Identify the blood parasite species.
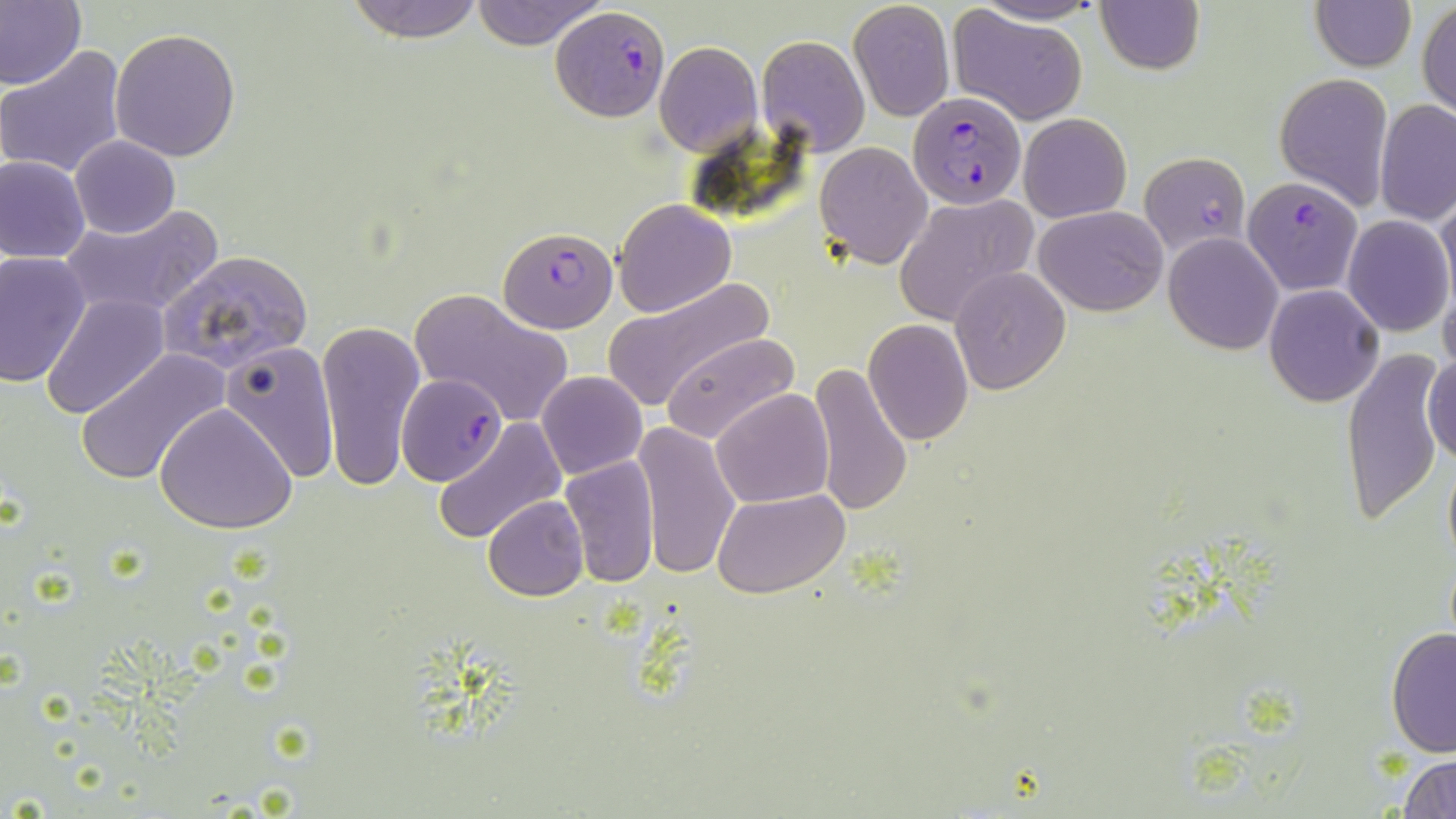

Plasmodium falciparum.

image_size: 1456×819 pixels
modality: optical microscopy
magnification: 1000x
stain: May-Grünwald-Giemsa
plasmodium_falciparum_infected_red_blood_cell_locations: 'approximate bounding boxes as (x1,y1)-(x2,y2) corner pairs in pixels: (553,9)-(668,122), (906,90)-(1027,210), (1139,152)-(1251,259), (1241,177)-(1363,294), (497,225)-(618,333), (398,373)-(506,485)'
preparation: thin blood film
field_of_view: single
uninfected_red_blood_cell_locations: 'approximate bounding boxes as (x1,y1)-(x2,y2) corner pairs in pixels: (0,0)-(85,92), (343,0)-(488,41), (469,0)-(604,48), (970,0)-(1105,25), (1095,0)-(1204,75), (1308,0)-(1416,71), (848,1)-(955,121), (1418,2)-(1455,121), (947,7)-(1091,126), (110,27)-(241,161), (755,34)-(869,156), (654,40)-(763,156), (0,46)-(129,179), (1276,72)-(1395,211), (1375,102)-(1456,226), (1018,112)-(1131,222), (69,137)-(179,239), (815,143)-(933,269), (1,155)-(90,264), (1437,192)-(1456,316), (893,195)-(1037,327), (612,198)-(737,318), (58,203)-(223,321), (1033,204)-(1169,315), (1341,214)-(1452,337), (1164,231)-(1284,355), (160,249)-(314,372), (0,251)-(93,389), (949,266)-(1071,393), (604,276)-(774,412), (1438,278)-(1456,381), (1264,284)-(1383,406), (410,288)-(571,425), (40,295)-(168,422), (316,319)-(426,492), (863,319)-(973,445), (660,332)-(800,446), (220,339)-(339,481), (1341,347)-(1446,529), (77,348)-(230,488), (1424,349)-(1456,469), (808,361)-(913,518), (535,370)-(648,480), (712,388)-(834,510), (154,403)-(296,535), (433,419)-(567,544), (633,421)-(741,582), (1441,451)-(1456,570), (560,456)-(659,589), (713,488)-(848,599), (482,496)-(590,602), (1386,626)-(1455,757), (1399,754)-(1456,818)'